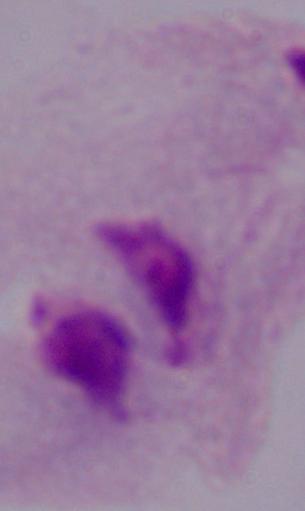
modality = photomicrograph
magnification = 1000x
identification = trichomonad